Identify the parasite.
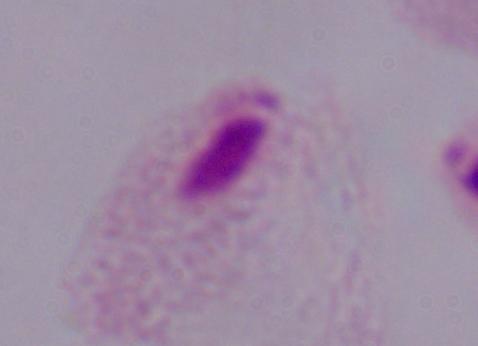

A trichomonad.

modality: micrograph
magnification: 1000x